Identify the blood parasite species.
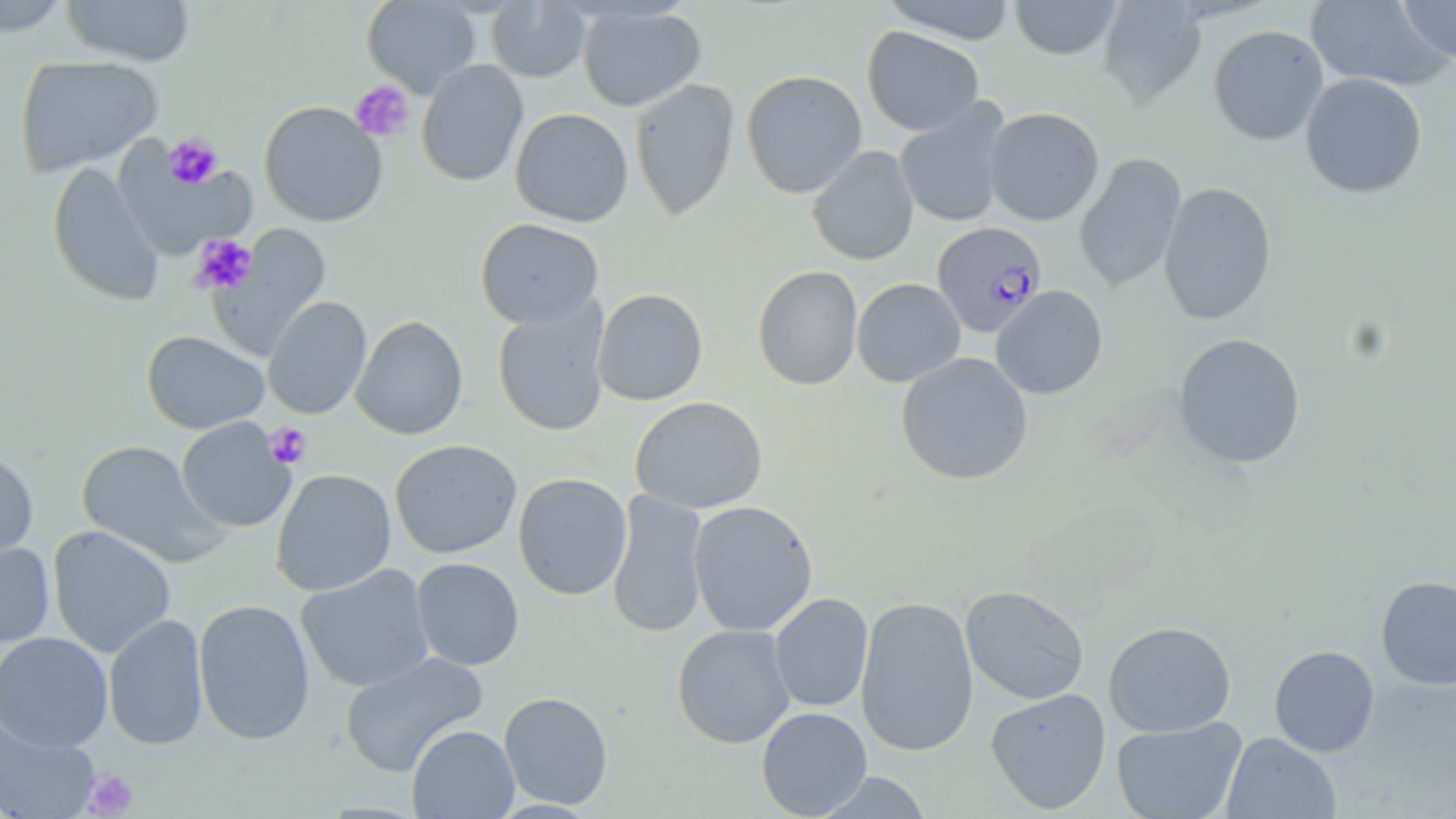
Plasmodium falciparum.

{
  "image_size": "1456×819 pixels",
  "uninfected_red_blood_cell_locations": "approximate bounding boxes as (x1,y1)-(x2,y2) corner pairs in pixels: (0,0)-(72,36), (60,0)-(195,66), (362,0)-(481,97), (879,0)-(1019,44), (1009,0)-(1124,60), (1306,0)-(1450,91), (1395,0)-(1456,65), (487,1)-(592,83), (1098,1)-(1207,107), (578,5)-(706,112), (1208,24)-(1328,146), (862,26)-(984,136), (15,55)-(163,176), (416,59)-(528,187), (741,70)-(867,198), (1300,72)-(1427,199), (630,78)-(740,221), (895,99)-(1010,228), (259,101)-(388,226), (984,107)-(1105,225), (510,108)-(634,226), (111,142)-(256,261), (807,145)-(919,265), (1075,152)-(1186,295), (47,161)-(165,305), (1158,181)-(1277,325), (475,218)-(604,329), (208,223)-(331,361), (752,265)-(863,391), (852,278)-(965,387), (991,285)-(1108,400), (592,288)-(707,406), (263,296)-(372,420), (493,298)-(611,437), (351,315)-(468,440), (141,330)-(270,435), (1173,332)-(1307,469), (895,352)-(1033,486), (629,396)-(768,514), (176,417)-(295,533), (76,439)-(229,568), (390,439)-(522,559), (0,450)-(38,567), (271,468)-(396,596), (513,472)-(632,600), (607,489)-(710,638), (688,500)-(818,637), (48,525)-(176,658), (0,542)-(55,647), (411,557)-(524,671), (296,563)-(435,693), (1376,575)-(1456,690), (960,585)-(1090,705), (769,593)-(874,712), (855,596)-(979,757), (193,599)-(315,745), (104,614)-(208,751), (1103,620)-(1236,737), (672,624)-(795,748), (0,632)-(113,753), (1269,644)-(1379,757), (340,651)-(489,777), (985,688)-(1111,814), (499,691)-(613,810), (756,707)-(872,818), (0,716)-(100,819), (1111,716)-(1247,819), (407,724)-(519,818), (1221,732)-(1341,819), (814,771)-(934,818)",
  "field_of_view": "single",
  "modality": "light microscopy",
  "stain": "May-Grünwald-Giemsa",
  "preparation": "thin blood smear",
  "magnification": "1000x",
  "platelet_locations": "approximate bounding boxes as (x1,y1)-(x2,y2) corner pairs in pixels: (350,81)-(414,142), (163,134)-(223,190), (190,234)-(257,294), (264,422)-(312,469), (82,769)-(139,817)",
  "plasmodium_falciparum_infected_red_blood_cell_locations": "approximate bounding boxes as (x1,y1)-(x2,y2) corner pairs in pixels: (932,221)-(1046,338)"
}